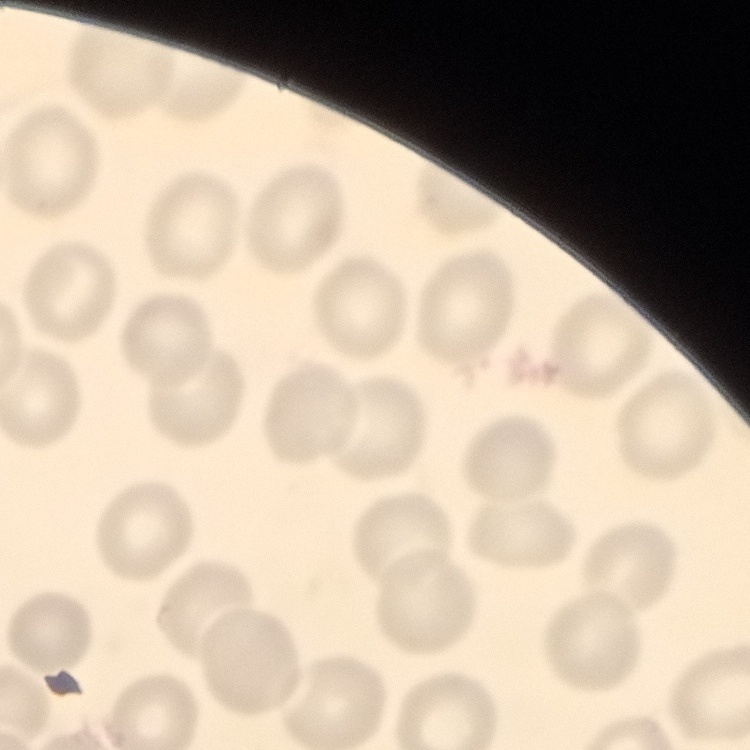

The red blood cells exhibit no rouleaux formation. Thin peripheral smear. One tile cut from a larger photomicrograph. Stained with either Field's or Giemsa.